Assess the morphology of the red blood cells.
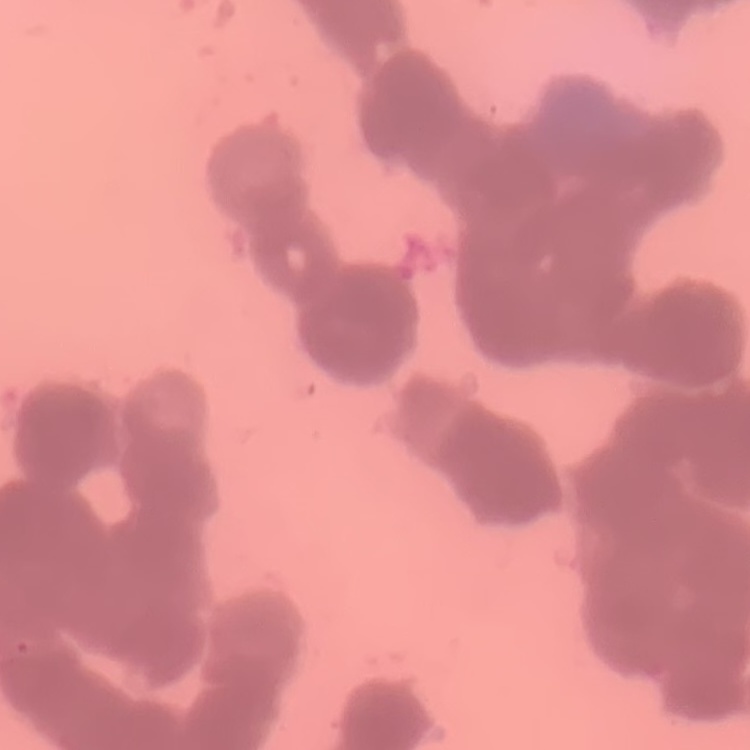
They show rouleaux formation.

preparation = thin peripheral smear
stain = Field's or Giemsa
image type = one tile cut from a larger photomicrograph